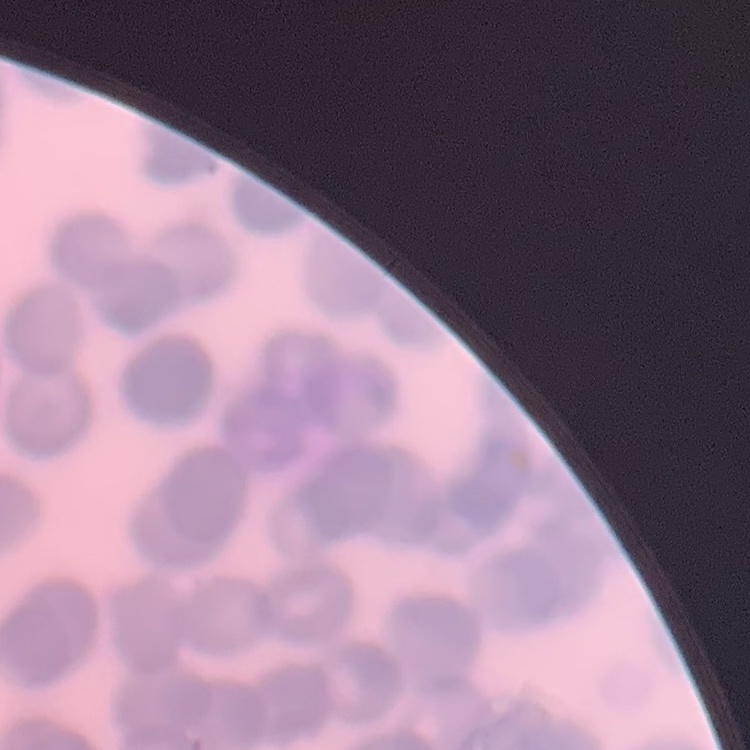 The erythrocytes show rouleaux formation. Square crop of a larger photomicrograph. Thin blood film. Field's or Giemsa stain.